Locate and identify every blood parasite.
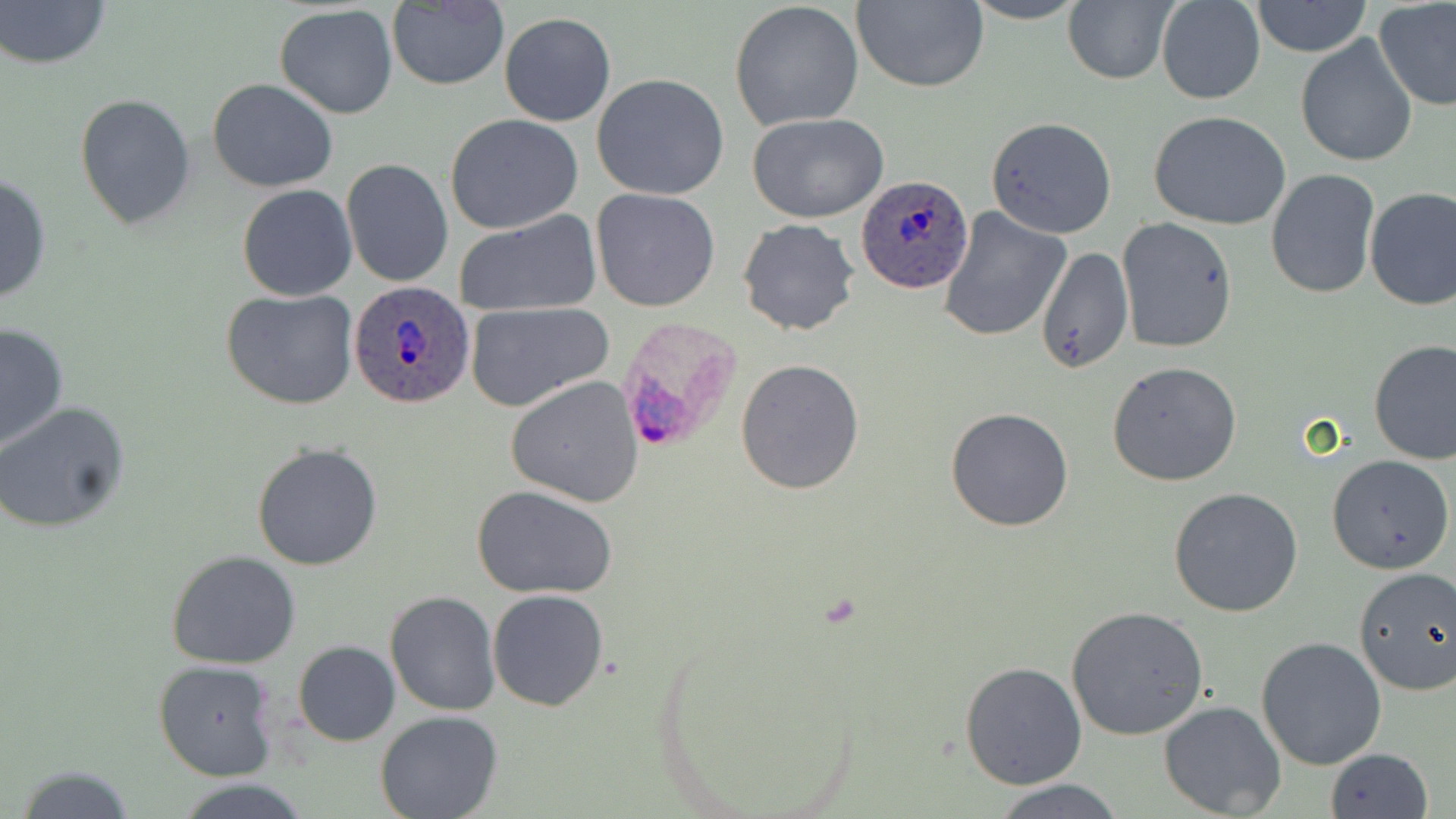

Approximate bounding boxes as named x1/y1/x2/y2 corners in pixels.
Plasmodium ovale-infected red blood cells: (x1=856, y1=175, x2=974, y2=294), (x1=347, y1=280, x2=474, y2=409), (x1=615, y1=317, x2=741, y2=458).
No Plasmodium falciparum, Plasmodium malariae, Plasmodium vivax, Babesia divergens, or Trypanosoma brucei observed.

Summary:
  - Uninfected red blood cell locations: (x1=1, y1=0, x2=114, y2=71), (x1=850, y1=0, x2=988, y2=93), (x1=961, y1=0, x2=1090, y2=25), (x1=1062, y1=0, x2=1179, y2=86), (x1=1156, y1=0, x2=1266, y2=106), (x1=728, y1=1, x2=864, y2=131), (x1=385, y1=2, x2=511, y2=90), (x1=1252, y1=2, x2=1370, y2=57), (x1=1374, y1=2, x2=1456, y2=111), (x1=274, y1=5, x2=399, y2=117), (x1=497, y1=12, x2=616, y2=126), (x1=1295, y1=34, x2=1417, y2=169), (x1=592, y1=73, x2=730, y2=200), (x1=208, y1=78, x2=338, y2=194), (x1=75, y1=93, x2=195, y2=228), (x1=1149, y1=109, x2=1292, y2=230), (x1=445, y1=113, x2=583, y2=235), (x1=747, y1=113, x2=889, y2=223), (x1=986, y1=116, x2=1116, y2=240), (x1=341, y1=158, x2=453, y2=288), (x1=1265, y1=168, x2=1380, y2=298), (x1=0, y1=171, x2=52, y2=307), (x1=237, y1=184, x2=357, y2=301), (x1=591, y1=187, x2=722, y2=312), (x1=1364, y1=188, x2=1456, y2=312), (x1=937, y1=207, x2=1071, y2=343), (x1=455, y1=212, x2=602, y2=317), (x1=738, y1=218, x2=858, y2=337), (x1=1116, y1=218, x2=1238, y2=352), (x1=1036, y1=246, x2=1132, y2=376), (x1=221, y1=289, x2=359, y2=411), (x1=464, y1=302, x2=615, y2=411), (x1=0, y1=322, x2=70, y2=453), (x1=1369, y1=339, x2=1456, y2=465), (x1=735, y1=359, x2=865, y2=496), (x1=1107, y1=361, x2=1242, y2=485), (x1=505, y1=375, x2=644, y2=507), (x1=0, y1=403, x2=131, y2=534), (x1=945, y1=408, x2=1074, y2=531), (x1=251, y1=443, x2=383, y2=570), (x1=1326, y1=454, x2=1454, y2=574), (x1=472, y1=484, x2=621, y2=600), (x1=1168, y1=487, x2=1303, y2=617), (x1=167, y1=550, x2=301, y2=669), (x1=1354, y1=567, x2=1456, y2=696), (x1=487, y1=590, x2=610, y2=711), (x1=386, y1=591, x2=500, y2=716), (x1=1066, y1=605, x2=1209, y2=740), (x1=1255, y1=636, x2=1387, y2=771), (x1=292, y1=641, x2=401, y2=747), (x1=153, y1=661, x2=278, y2=781), (x1=960, y1=661, x2=1088, y2=790), (x1=1158, y1=700, x2=1287, y2=818), (x1=374, y1=710, x2=504, y2=819), (x1=1324, y1=747, x2=1433, y2=819), (x1=13, y1=764, x2=141, y2=819), (x1=989, y1=778, x2=1132, y2=817), (x1=173, y1=779, x2=314, y2=819)
  - Slide-level diagnosis: Plasmodium ovale
  - Field of view: one of a larger specimen
  - Modality: light microscopy
  - Stain: May-Grünwald-Giemsa
  - Magnification: 1000x
  - Image size: 1456×819 pixels
  - Preparation: thin blood film